Describe the morphology of the red blood cells.
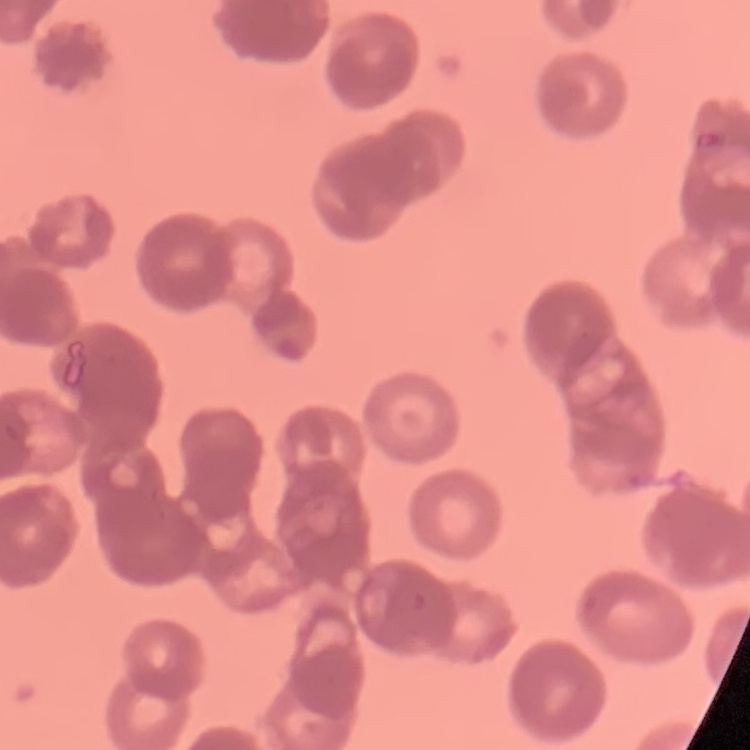

They show rouleaux formation.

Stained with either Field's or Giemsa. Square crop of a larger photomicrograph. Thin blood film.